State which parasite is depicted.
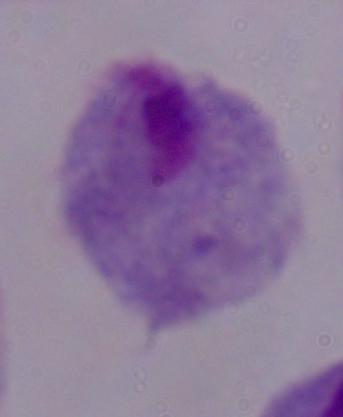

This is a trichomonad.

1000x magnification. Photomicrograph.